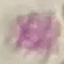
{
  "malaria_status": "uninfected",
  "preparation": "thin blood smear",
  "stain": "Giemsa",
  "capture": "smartphone through the microscope eyepiece",
  "image_type": "automatically extracted cell patch, resized to 64 × 64 pixels"
}